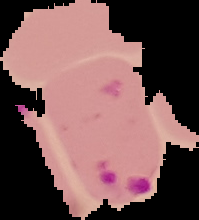
Summary:
  - Result: Plasmodium parasites identified
  - Image type: cell region segmented out of the field of view; surrounding area masked to black
  - Image size: 199×220 pixels
  - Preparation: thin blood film